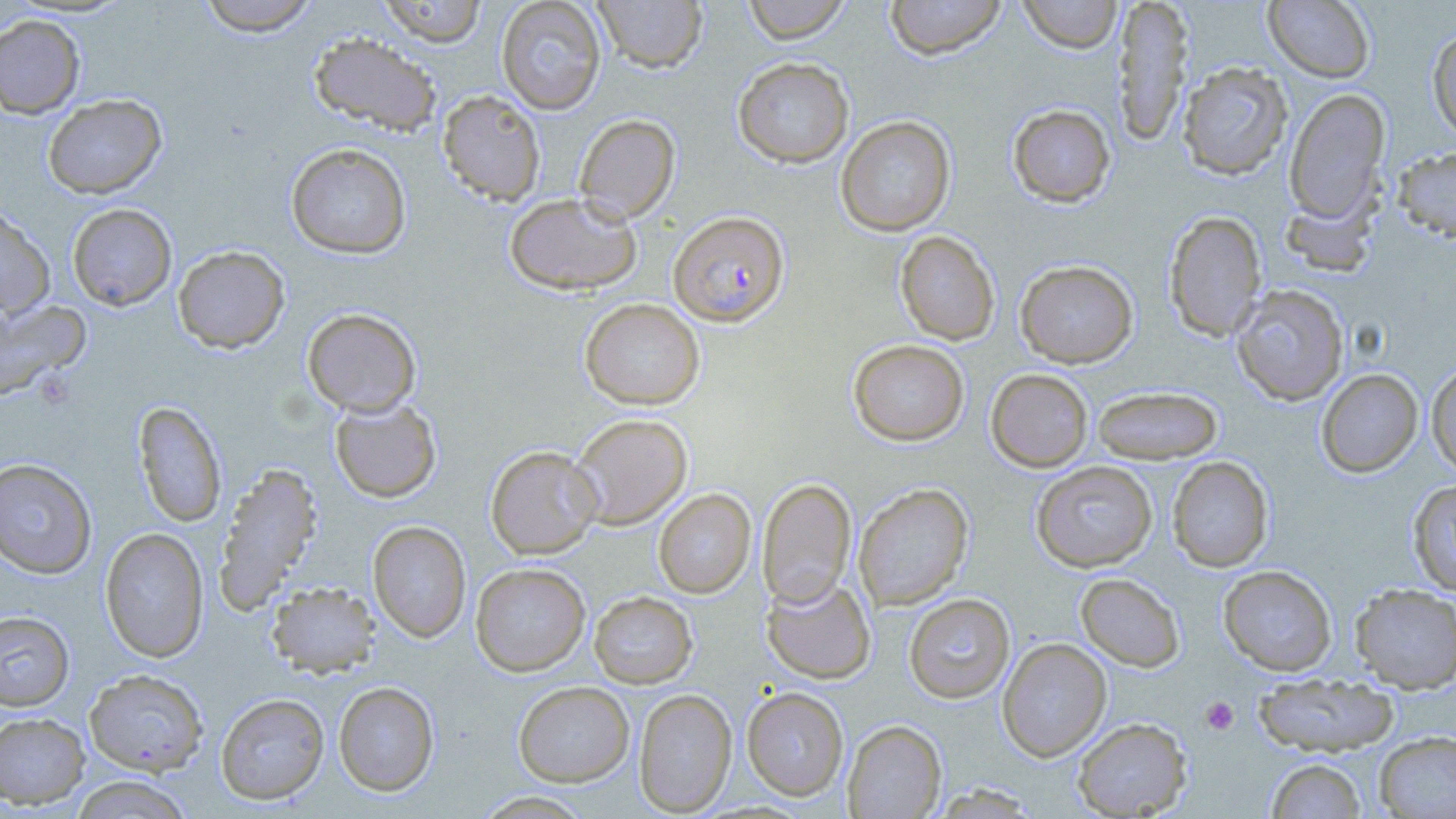
Summary:
  - Coordinate format: approximate bounding boxes as (x1, y1, x2, y2) in pixels
  - Platelet locations: (1200, 696, 1239, 736)
  - Plasmodium falciparum-infected red blood cell locations: (669, 211, 789, 326)
  - Uninfected red blood cell locations: (195, 0, 321, 36), (377, 0, 489, 47), (496, 0, 606, 115), (593, 0, 708, 73), (742, 0, 851, 43), (884, 0, 1007, 59), (1018, 0, 1122, 53), (1112, 0, 1193, 149), (1263, 0, 1375, 83), (0, 15, 86, 119), (1427, 28, 1456, 144), (308, 32, 442, 137), (732, 57, 854, 168), (1177, 61, 1293, 180), (1284, 88, 1391, 223), (437, 90, 546, 206), (42, 94, 167, 199), (1007, 104, 1116, 207), (573, 114, 680, 222), (835, 115, 956, 236), (286, 142, 412, 259), (1393, 147, 1456, 243), (1280, 189, 1381, 278), (504, 192, 641, 295), (66, 203, 177, 311), (0, 206, 55, 319), (1163, 210, 1267, 342), (895, 230, 1000, 345), (172, 245, 290, 353), (1015, 259, 1138, 368), (1230, 284, 1349, 406), (0, 298, 91, 402), (579, 298, 705, 410), (302, 307, 422, 417), (848, 339, 969, 446), (1426, 361, 1456, 477), (985, 368, 1093, 473), (1316, 369, 1423, 477), (1092, 386, 1223, 464), (329, 398, 441, 503), (133, 401, 227, 527), (569, 412, 693, 530), (485, 445, 602, 559), (1167, 456, 1274, 572), (0, 458, 98, 579), (1031, 461, 1158, 572), (214, 462, 324, 612), (757, 477, 857, 608), (1408, 480, 1456, 596), (853, 482, 974, 610), (653, 488, 756, 598), (368, 520, 471, 643), (99, 527, 209, 662), (471, 562, 591, 676), (1218, 565, 1337, 676), (1075, 573, 1185, 671), (761, 575, 876, 684), (266, 581, 381, 677), (1350, 583, 1456, 693), (589, 591, 698, 688), (903, 593, 1015, 703), (0, 610, 74, 711), (997, 637, 1112, 761), (84, 669, 209, 775), (1252, 672, 1399, 756), (333, 681, 440, 797), (514, 681, 634, 786), (742, 686, 849, 801), (633, 688, 737, 816), (215, 693, 329, 804), (0, 711, 90, 809), (1072, 717, 1192, 818), (842, 719, 947, 818), (1374, 731, 1456, 818), (1265, 758, 1367, 819), (68, 776, 195, 818), (473, 790, 595, 818)
  - Slide-level diagnosis: Plasmodium falciparum
  - Preparation: thin blood film
  - Modality: light microscopy
  - Field of view: one of a larger specimen
  - Magnification: 1000x
  - Stain: May-Grünwald-Giemsa
  - Image size: 1456×819 pixels